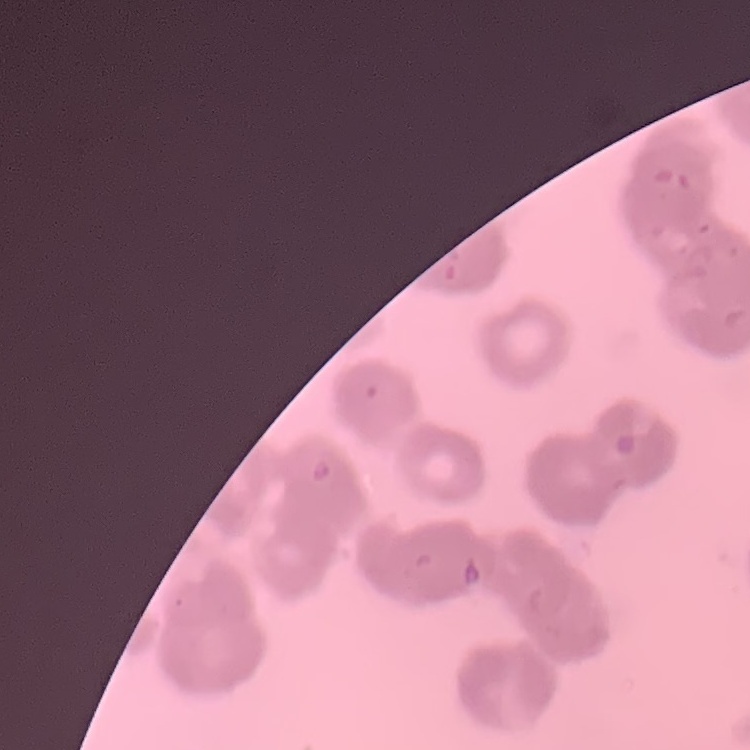

red blood cell morphology = rouleaux formation
image type = one tile cut from a larger photomicrograph
preparation = thin blood film
stain = Field's or Giemsa